Assess this cell for malaria.
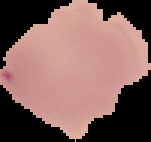

Uninfected.

Image is 151×142 pixels. From a thin blood smear. Segmented cell region on a black background.